Identify the parasite.
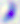
This is Toxoplasma gondii.

Summary:
  - Modality: micrograph
  - Magnification: 400x